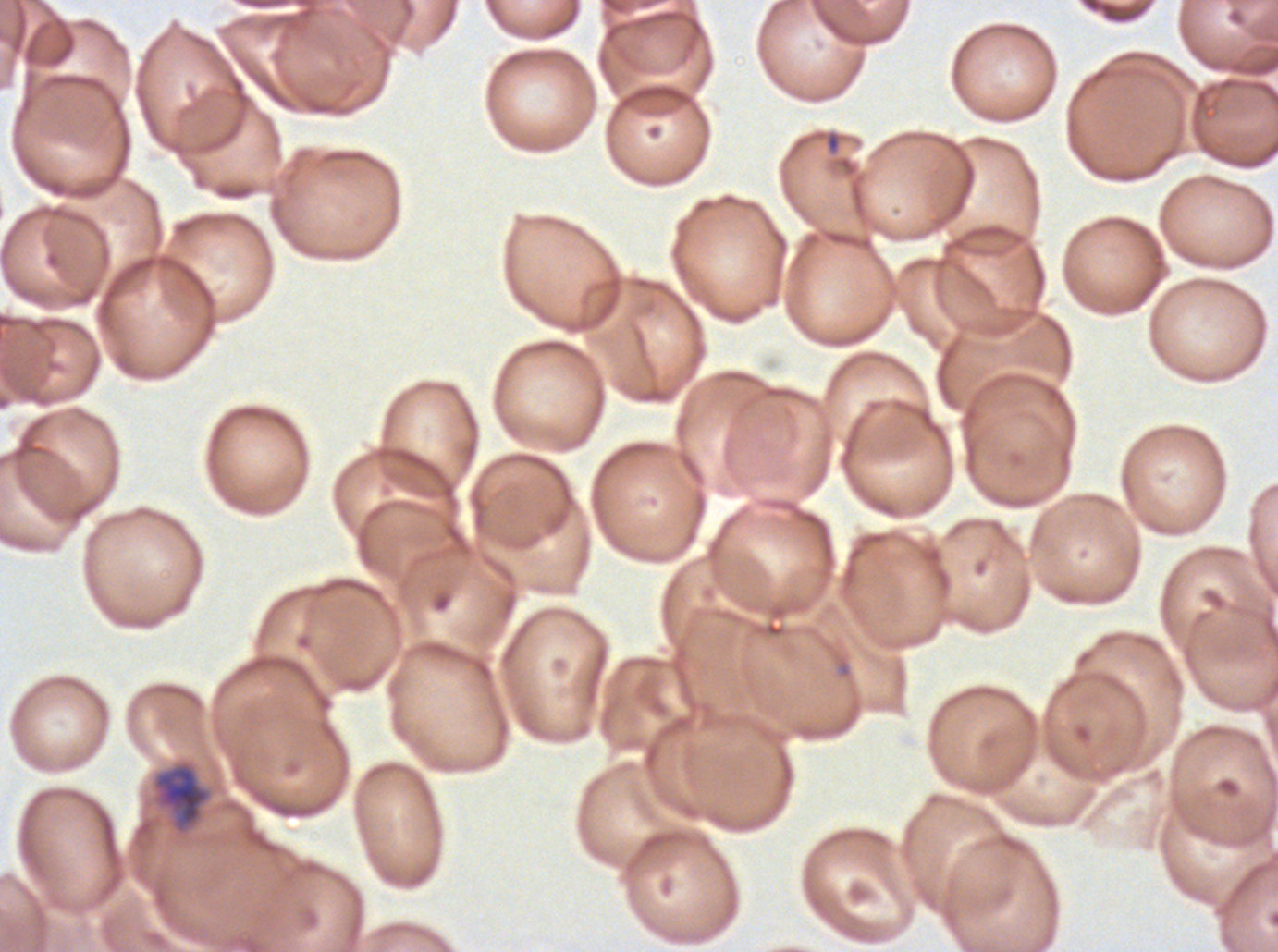 Approximate bounding boxes as (x1, y1, x2, y2) in pixels. Mid trophozoite locations: (153, 763, 211, 832). Thin blood smear. Giemsa stain. One sub-image of a larger composite. Ex-vivo Plasmodium falciparum culture from a patient in The Gambia, grown for 24 to 48 hours. Image is 1278×952 pixels.